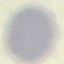
{
  "result": "no malaria parasites detected",
  "capture": "smartphone camera at the microscope eyepiece",
  "image_type": "automatically extracted cell patch, resized to 64 × 64 pixels",
  "preparation": "thin blood smear",
  "stain": "Giemsa"
}